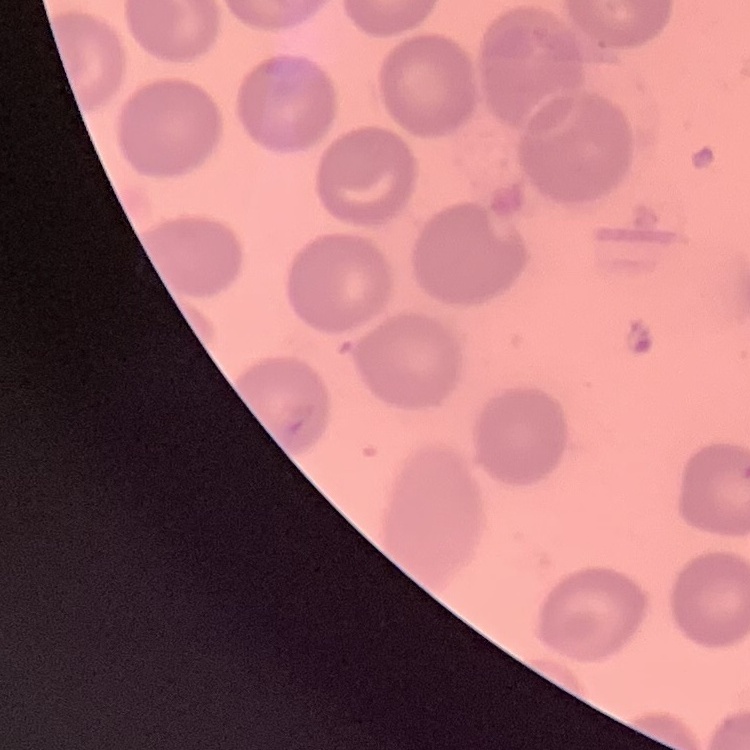
The erythrocytes show no rouleaux formation. One tile cut from a larger photomicrograph. Stained with either Field's or Giemsa. Thin blood smear.